Identify the blood parasite species.
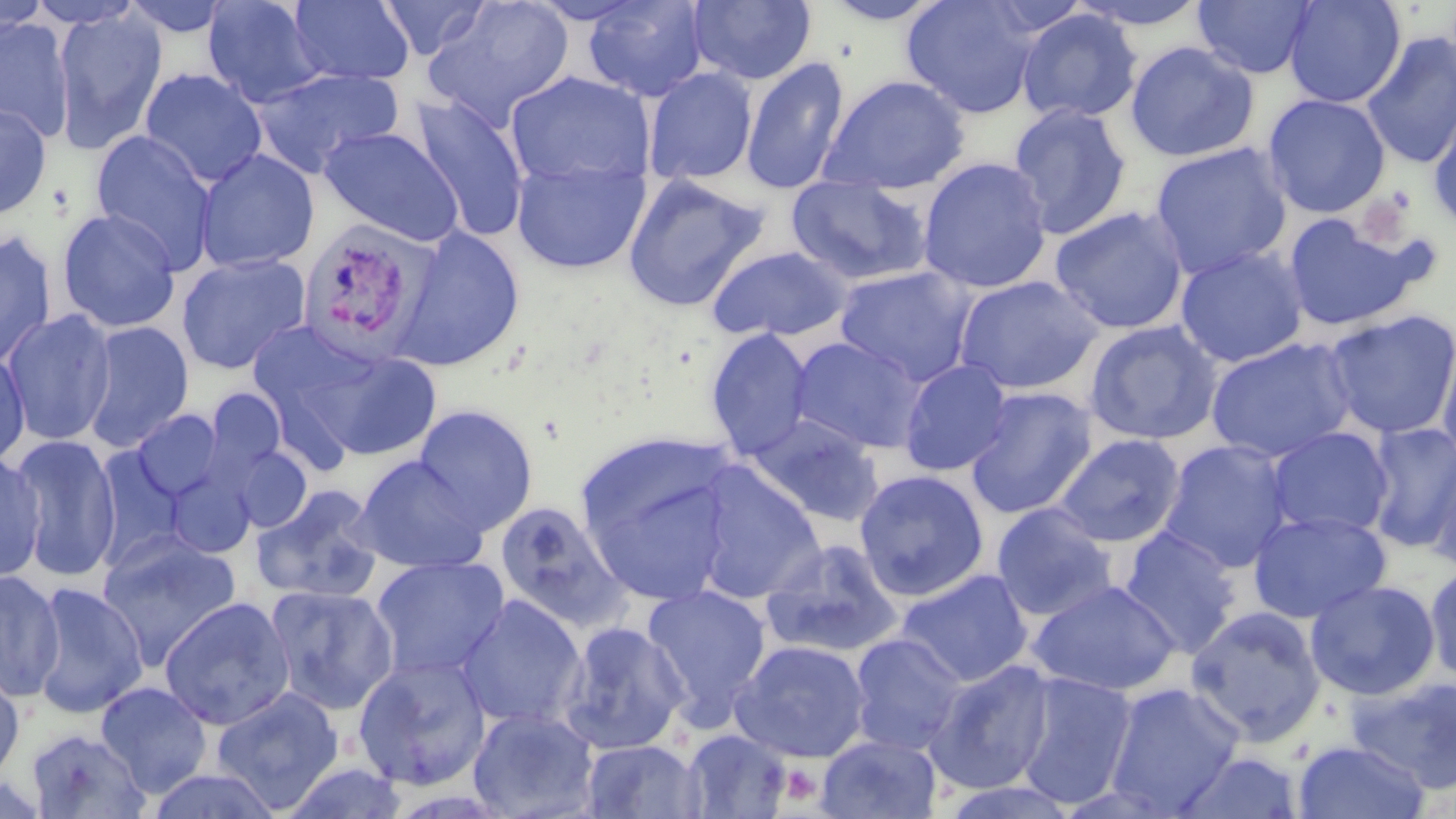
Plasmodium vivax.

{
  "modality": "light microscopy",
  "stain": "May-Grünwald-Giemsa",
  "plasmodium_vivax_infected_red_blood_cell_locations": "approximate bounding boxes as named x1/y1/x2/y2 corners in pixels: (x1=295, y1=218, x2=438, y2=365)",
  "preparation": "thin blood smear",
  "uninfected_red_blood_cell_locations": "approximate bounding boxes as named x1/y1/x2/y2 corners in pixels: (x1=119, y1=0, x2=237, y2=39), (x1=201, y1=0, x2=328, y2=108), (x1=288, y1=0, x2=415, y2=86), (x1=377, y1=0, x2=491, y2=61), (x1=421, y1=0, x2=575, y2=131), (x1=581, y1=0, x2=709, y2=102), (x1=819, y1=0, x2=949, y2=25), (x1=901, y1=0, x2=1043, y2=119), (x1=1066, y1=0, x2=1212, y2=31), (x1=1193, y1=0, x2=1318, y2=79), (x1=1283, y1=0, x2=1406, y2=108), (x1=688, y1=1, x2=816, y2=85), (x1=0, y1=2, x2=52, y2=41), (x1=53, y1=6, x2=169, y2=155), (x1=1017, y1=9, x2=1142, y2=124), (x1=0, y1=16, x2=75, y2=143), (x1=1360, y1=32, x2=1456, y2=169), (x1=1124, y1=41, x2=1260, y2=162), (x1=740, y1=56, x2=850, y2=195), (x1=642, y1=67, x2=758, y2=186), (x1=139, y1=68, x2=268, y2=189), (x1=250, y1=68, x2=403, y2=177), (x1=504, y1=70, x2=658, y2=193), (x1=819, y1=74, x2=970, y2=195), (x1=408, y1=93, x2=530, y2=243), (x1=1263, y1=93, x2=1391, y2=218), (x1=1427, y1=101, x2=1456, y2=230), (x1=0, y1=102, x2=53, y2=221), (x1=1007, y1=103, x2=1132, y2=239), (x1=318, y1=125, x2=464, y2=247), (x1=89, y1=129, x2=217, y2=271), (x1=1150, y1=142, x2=1293, y2=280), (x1=194, y1=147, x2=320, y2=273), (x1=511, y1=156, x2=650, y2=274), (x1=918, y1=156, x2=1052, y2=293), (x1=622, y1=173, x2=769, y2=311), (x1=786, y1=176, x2=932, y2=286), (x1=1050, y1=205, x2=1190, y2=335), (x1=56, y1=208, x2=181, y2=334), (x1=1283, y1=213, x2=1428, y2=333), (x1=391, y1=227, x2=525, y2=371), (x1=0, y1=231, x2=58, y2=369), (x1=707, y1=245, x2=852, y2=343), (x1=1175, y1=246, x2=1308, y2=367), (x1=176, y1=251, x2=311, y2=375), (x1=834, y1=266, x2=977, y2=386), (x1=954, y1=274, x2=1105, y2=395), (x1=2, y1=308, x2=118, y2=446), (x1=1322, y1=308, x2=1456, y2=440), (x1=79, y1=320, x2=195, y2=453), (x1=1083, y1=320, x2=1223, y2=446), (x1=704, y1=327, x2=814, y2=460), (x1=1437, y1=329, x2=1456, y2=473), (x1=788, y1=336, x2=928, y2=453), (x1=1206, y1=337, x2=1357, y2=463), (x1=306, y1=345, x2=443, y2=461), (x1=0, y1=349, x2=31, y2=470), (x1=898, y1=359, x2=1013, y2=476), (x1=964, y1=386, x2=1098, y2=519), (x1=199, y1=387, x2=289, y2=492), (x1=412, y1=404, x2=538, y2=534), (x1=130, y1=408, x2=225, y2=502), (x1=748, y1=414, x2=885, y2=526), (x1=1364, y1=422, x2=1456, y2=554), (x1=1266, y1=427, x2=1394, y2=539), (x1=9, y1=433, x2=122, y2=582), (x1=1053, y1=433, x2=1186, y2=548), (x1=1159, y1=439, x2=1294, y2=574), (x1=577, y1=440, x2=738, y2=606), (x1=225, y1=443, x2=313, y2=532), (x1=90, y1=444, x2=190, y2=571), (x1=0, y1=451, x2=47, y2=584), (x1=1426, y1=451, x2=1456, y2=574), (x1=352, y1=455, x2=488, y2=574), (x1=692, y1=464, x2=825, y2=604), (x1=854, y1=468, x2=990, y2=601), (x1=250, y1=484, x2=386, y2=605), (x1=493, y1=499, x2=630, y2=632), (x1=992, y1=503, x2=1118, y2=622), (x1=1247, y1=510, x2=1391, y2=623), (x1=1119, y1=526, x2=1243, y2=658), (x1=95, y1=531, x2=244, y2=670), (x1=760, y1=537, x2=904, y2=659), (x1=370, y1=554, x2=509, y2=680), (x1=1425, y1=561, x2=1456, y2=687), (x1=0, y1=568, x2=65, y2=703), (x1=897, y1=568, x2=1033, y2=687), (x1=1027, y1=579, x2=1181, y2=696), (x1=1305, y1=579, x2=1440, y2=700), (x1=29, y1=581, x2=149, y2=718), (x1=641, y1=583, x2=772, y2=725), (x1=264, y1=584, x2=399, y2=715), (x1=456, y1=594, x2=588, y2=730), (x1=159, y1=596, x2=296, y2=730), (x1=1185, y1=605, x2=1327, y2=745), (x1=557, y1=620, x2=689, y2=754), (x1=849, y1=633, x2=966, y2=755), (x1=731, y1=641, x2=871, y2=763), (x1=352, y1=653, x2=493, y2=792), (x1=926, y1=659, x2=1057, y2=795), (x1=0, y1=669, x2=26, y2=785), (x1=1015, y1=671, x2=1138, y2=809), (x1=1347, y1=673, x2=1456, y2=793), (x1=95, y1=681, x2=213, y2=797), (x1=1104, y1=681, x2=1245, y2=815), (x1=210, y1=687, x2=344, y2=812), (x1=467, y1=707, x2=600, y2=819), (x1=24, y1=727, x2=151, y2=818), (x1=682, y1=729, x2=792, y2=818), (x1=816, y1=734, x2=942, y2=818), (x1=581, y1=739, x2=706, y2=818), (x1=1292, y1=740, x2=1430, y2=819), (x1=1172, y1=750, x2=1306, y2=817), (x1=144, y1=767, x2=284, y2=818)",
  "platelet_locations": "approximate bounding boxes as named x1/y1/x2/y2 corners in pixels: (x1=1352, y1=187, x2=1420, y2=252), (x1=778, y1=763, x2=823, y2=805)",
  "magnification": "1000x",
  "image_size": "1456×819 pixels",
  "field_of_view": "one of a larger specimen"
}